Classify this cell by malaria status.
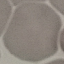
Uninfected.

stain: Giemsa
capture: smartphone through the microscope eyepiece
image_type: automatically extracted cell patch, resized to 64 × 64 pixels
preparation: thin smear